State which parasite is depicted.
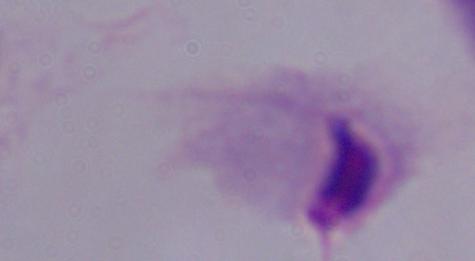

A trichomonad.

magnification = 1000x
modality = photomicrograph